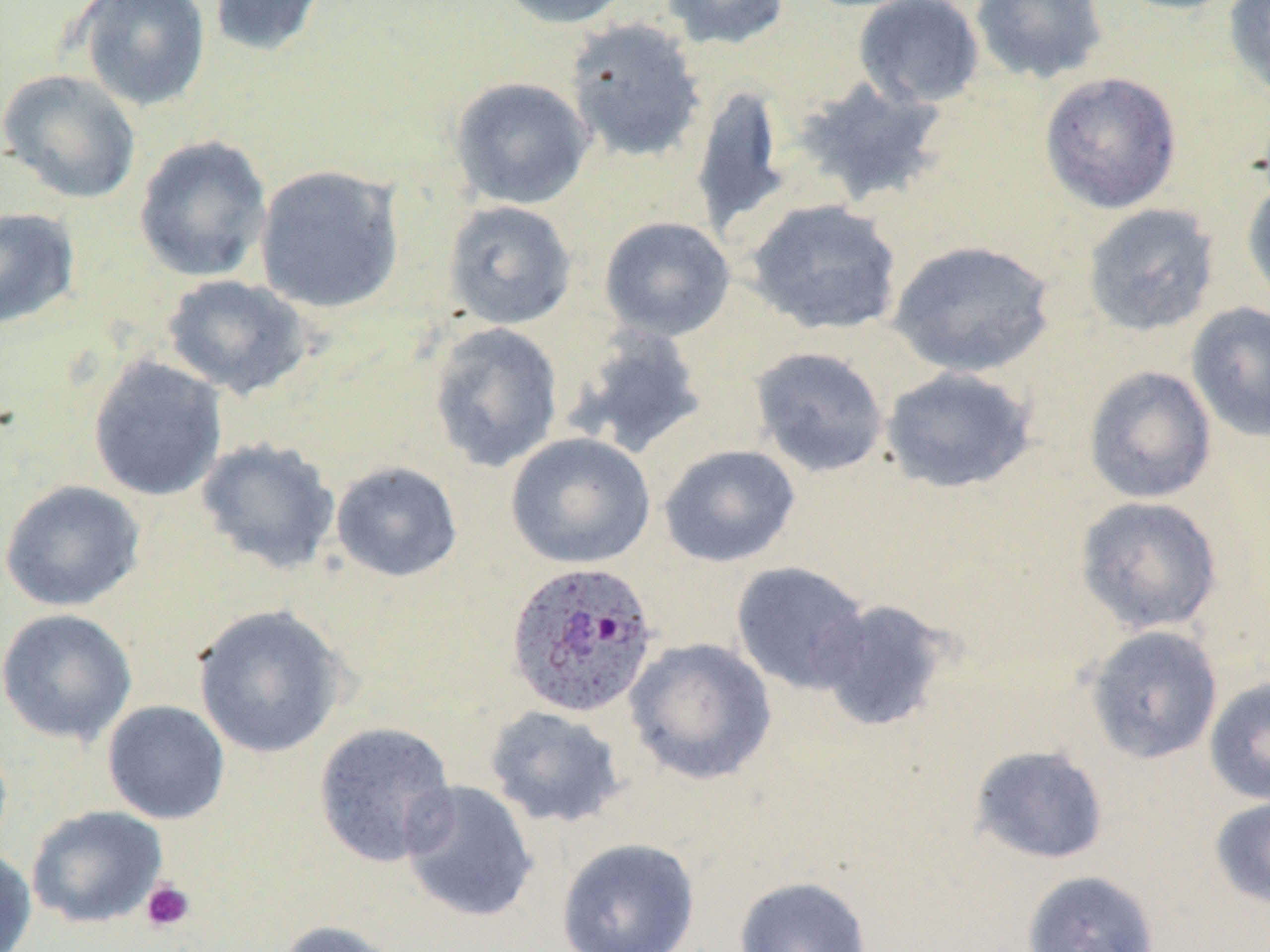
Approximate bounding boxes as (x1,y1)-(x2,y2) corner pairs in pixels. Platelet locations: (140,879)-(196,933). Uninfected red blood cell locations: (76,0)-(211,112), (208,0)-(327,58), (496,0)-(634,29), (660,0)-(791,51), (853,0)-(985,109), (970,0)-(1108,85), (1106,0)-(1247,16), (1223,0)-(1270,99), (564,18)-(707,164), (1,69)-(141,204), (1039,71)-(1182,214), (792,75)-(951,208), (449,76)-(594,210), (690,84)-(791,238), (133,135)-(273,284), (254,164)-(405,314), (1241,174)-(1270,312), (745,199)-(903,336), (443,200)-(577,330), (1081,202)-(1221,338), (0,206)-(81,330), (599,216)-(735,341), (888,239)-(1056,378), (162,274)-(314,400), (1186,301)-(1270,442), (427,321)-(564,472), (566,325)-(708,459), (749,346)-(890,478), (87,355)-(227,502), (1083,365)-(1217,504), (880,366)-(1038,495), (506,432)-(656,570), (195,437)-(341,575), (659,444)-(801,568), (330,460)-(463,583), (0,479)-(146,612), (1074,495)-(1224,635), (730,561)-(871,694), (813,598)-(953,733), (192,603)-(348,758), (0,608)-(137,745), (1084,625)-(1223,764), (625,637)-(778,786), (1204,678)-(1270,806), (102,700)-(230,825), (484,705)-(627,829), (312,721)-(458,868), (968,744)-(1109,865), (399,780)-(539,923), (1209,795)-(1270,909), (26,805)-(168,929), (556,837)-(701,951), (0,846)-(36,952), (1021,869)-(1160,952), (733,875)-(872,952), (274,919)-(406,952). Plasmodium ovale-infected red blood cell locations: (508,557)-(663,716). Slide-level diagnosis: Plasmodium ovale. Thin blood film. 1000x magnification. May-Grünwald-Giemsa stain. Optical microscopy. Single field of view. Image is 1270×952 pixels.